State the blood parasite species.
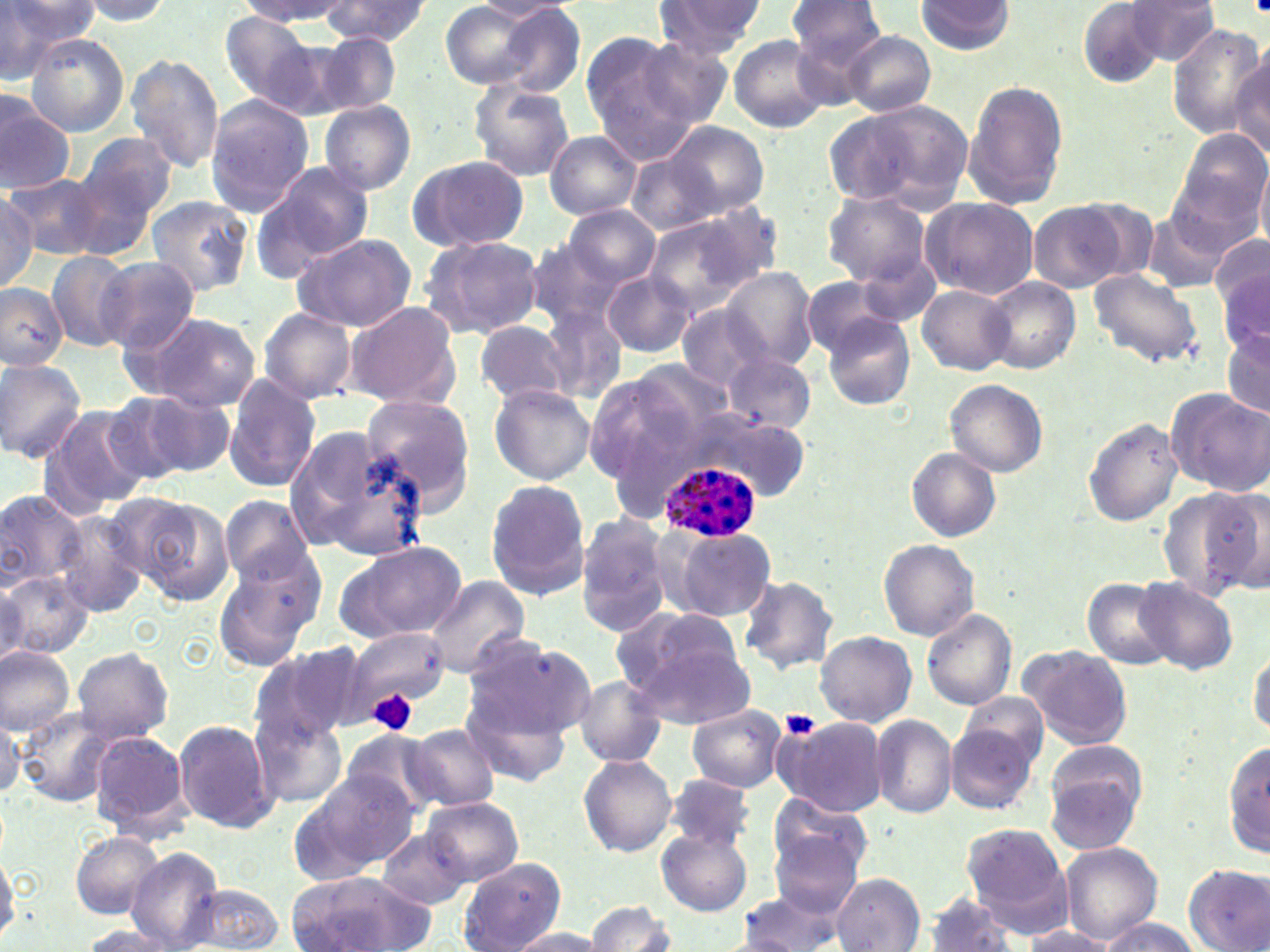

Plasmodium ovale.

Summary:
  - Coordinate format: approximate bounding boxes as named x1/y1/x2/y2 corners in pixels
  - Platelet locations: (x1=367, y1=689, x2=418, y2=738), (x1=781, y1=709, x2=820, y2=740)
  - Plasmodium ovale-infected red blood cell locations: (x1=659, y1=459, x2=762, y2=543)
  - Uninfected red blood cell locations: (x1=0, y1=0, x2=92, y2=76), (x1=322, y1=0, x2=430, y2=47), (x1=916, y1=0, x2=1014, y2=56), (x1=73, y1=1, x2=175, y2=24), (x1=238, y1=1, x2=359, y2=23), (x1=651, y1=1, x2=765, y2=61), (x1=785, y1=1, x2=888, y2=68), (x1=1123, y1=1, x2=1220, y2=66), (x1=438, y1=2, x2=544, y2=89), (x1=474, y1=2, x2=581, y2=22), (x1=1078, y1=3, x2=1164, y2=87), (x1=491, y1=5, x2=587, y2=98), (x1=218, y1=12, x2=328, y2=111), (x1=1168, y1=24, x2=1267, y2=139), (x1=579, y1=28, x2=705, y2=152), (x1=845, y1=30, x2=936, y2=117), (x1=24, y1=33, x2=130, y2=136), (x1=314, y1=33, x2=401, y2=116), (x1=728, y1=36, x2=833, y2=133), (x1=639, y1=38, x2=733, y2=129), (x1=1231, y1=48, x2=1270, y2=159), (x1=126, y1=54, x2=224, y2=175), (x1=963, y1=78, x2=1070, y2=210), (x1=468, y1=80, x2=575, y2=182), (x1=204, y1=96, x2=316, y2=215), (x1=841, y1=98, x2=974, y2=208), (x1=319, y1=100, x2=416, y2=196), (x1=1, y1=101, x2=75, y2=195), (x1=0, y1=105, x2=141, y2=202), (x1=665, y1=121, x2=770, y2=217), (x1=1174, y1=129, x2=1269, y2=232), (x1=76, y1=131, x2=180, y2=230), (x1=545, y1=132, x2=640, y2=219), (x1=625, y1=154, x2=725, y2=236), (x1=408, y1=155, x2=531, y2=252), (x1=252, y1=158, x2=376, y2=277), (x1=1255, y1=158, x2=1270, y2=251), (x1=1167, y1=167, x2=1266, y2=263), (x1=8, y1=174, x2=101, y2=258), (x1=822, y1=191, x2=931, y2=287), (x1=0, y1=192, x2=39, y2=292), (x1=146, y1=195, x2=253, y2=296), (x1=919, y1=196, x2=1038, y2=300), (x1=1069, y1=196, x2=1158, y2=285), (x1=1030, y1=202, x2=1125, y2=292), (x1=565, y1=205, x2=660, y2=287), (x1=641, y1=207, x2=775, y2=312), (x1=1142, y1=212, x2=1230, y2=293), (x1=290, y1=233, x2=416, y2=332), (x1=1210, y1=234, x2=1269, y2=315), (x1=420, y1=235, x2=544, y2=339), (x1=526, y1=242, x2=632, y2=333), (x1=47, y1=251, x2=135, y2=350), (x1=96, y1=257, x2=199, y2=354), (x1=720, y1=266, x2=819, y2=369), (x1=1086, y1=268, x2=1205, y2=370), (x1=601, y1=272, x2=699, y2=357), (x1=1217, y1=273, x2=1269, y2=358), (x1=982, y1=277, x2=1079, y2=374), (x1=801, y1=279, x2=900, y2=358), (x1=0, y1=282, x2=69, y2=370), (x1=917, y1=284, x2=1015, y2=375), (x1=344, y1=300, x2=462, y2=411), (x1=676, y1=305, x2=767, y2=393), (x1=541, y1=307, x2=629, y2=405), (x1=259, y1=308, x2=358, y2=403), (x1=136, y1=311, x2=262, y2=412), (x1=822, y1=311, x2=914, y2=409), (x1=474, y1=320, x2=572, y2=405), (x1=1219, y1=326, x2=1269, y2=419), (x1=179, y1=333, x2=314, y2=482), (x1=725, y1=352, x2=816, y2=433), (x1=0, y1=358, x2=87, y2=463), (x1=583, y1=366, x2=725, y2=487), (x1=224, y1=373, x2=321, y2=493), (x1=944, y1=378, x2=1049, y2=476), (x1=489, y1=384, x2=595, y2=485), (x1=1167, y1=388, x2=1268, y2=493), (x1=138, y1=390, x2=234, y2=478), (x1=97, y1=393, x2=202, y2=486), (x1=360, y1=396, x2=477, y2=514), (x1=39, y1=403, x2=149, y2=521), (x1=687, y1=411, x2=808, y2=502), (x1=1084, y1=418, x2=1184, y2=525), (x1=284, y1=423, x2=431, y2=563), (x1=907, y1=448, x2=1001, y2=543), (x1=485, y1=481, x2=591, y2=601), (x1=1159, y1=487, x2=1269, y2=597), (x1=0, y1=489, x2=86, y2=591), (x1=119, y1=493, x2=235, y2=605), (x1=219, y1=495, x2=314, y2=586), (x1=55, y1=511, x2=147, y2=617), (x1=575, y1=513, x2=673, y2=637), (x1=664, y1=523, x2=775, y2=622), (x1=880, y1=539, x2=981, y2=640), (x1=336, y1=541, x2=465, y2=643), (x1=214, y1=552, x2=324, y2=672), (x1=2, y1=573, x2=92, y2=657), (x1=737, y1=573, x2=839, y2=674), (x1=1135, y1=576, x2=1238, y2=675), (x1=421, y1=577, x2=529, y2=678), (x1=1082, y1=578, x2=1175, y2=669), (x1=0, y1=582, x2=30, y2=669), (x1=616, y1=606, x2=754, y2=723), (x1=921, y1=609, x2=1017, y2=710), (x1=344, y1=621, x2=446, y2=717), (x1=463, y1=631, x2=592, y2=747), (x1=814, y1=631, x2=916, y2=725), (x1=250, y1=643, x2=366, y2=746), (x1=1249, y1=643, x2=1270, y2=739), (x1=0, y1=645, x2=77, y2=735), (x1=1019, y1=645, x2=1133, y2=750), (x1=71, y1=647, x2=175, y2=744), (x1=574, y1=675, x2=667, y2=767), (x1=461, y1=682, x2=577, y2=786), (x1=960, y1=692, x2=1049, y2=771), (x1=687, y1=704, x2=785, y2=793), (x1=0, y1=710, x2=23, y2=801), (x1=19, y1=711, x2=118, y2=806), (x1=251, y1=714, x2=347, y2=809), (x1=775, y1=715, x2=889, y2=817), (x1=870, y1=715, x2=957, y2=819), (x1=174, y1=719, x2=279, y2=834), (x1=402, y1=724, x2=500, y2=812), (x1=947, y1=724, x2=1039, y2=813), (x1=339, y1=729, x2=445, y2=819), (x1=88, y1=730, x2=191, y2=837), (x1=1224, y1=739, x2=1270, y2=859), (x1=1042, y1=748, x2=1148, y2=855), (x1=578, y1=753, x2=677, y2=857), (x1=295, y1=769, x2=422, y2=877), (x1=666, y1=773, x2=755, y2=849), (x1=770, y1=794, x2=871, y2=885), (x1=420, y1=796, x2=524, y2=887), (x1=961, y1=822, x2=1074, y2=934), (x1=657, y1=826, x2=752, y2=916), (x1=376, y1=829, x2=473, y2=910), (x1=769, y1=830, x2=863, y2=918), (x1=69, y1=831, x2=164, y2=921), (x1=1060, y1=842, x2=1162, y2=945), (x1=126, y1=846, x2=224, y2=951), (x1=0, y1=849, x2=22, y2=944), (x1=457, y1=858, x2=567, y2=952), (x1=1185, y1=865, x2=1269, y2=951), (x1=287, y1=872, x2=441, y2=950), (x1=831, y1=873, x2=924, y2=951), (x1=184, y1=883, x2=285, y2=951), (x1=734, y1=889, x2=847, y2=951), (x1=922, y1=894, x2=1018, y2=952), (x1=585, y1=899, x2=675, y2=952), (x1=1098, y1=918, x2=1205, y2=952), (x1=1019, y1=925, x2=1116, y2=951), (x1=76, y1=926, x2=182, y2=951), (x1=504, y1=928, x2=607, y2=951)
  - Image size: 1270×952 pixels
  - Stain: May-Grünwald-Giemsa
  - Magnification: 1000x
  - Preparation: thin blood smear
  - Field of view: one of a larger specimen
  - Modality: light microscopy